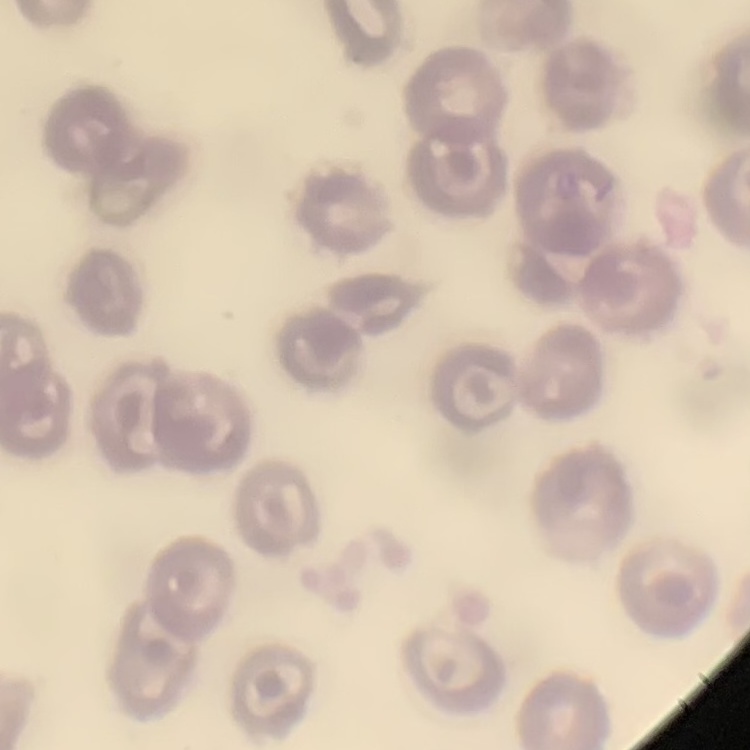

{
  "red_blood_cell_morphology": "no rouleaux formation",
  "preparation": "thin blood smear",
  "stain": "Field's or Giemsa",
  "image_type": "square crop of a larger photomicrograph"
}